Assess this cell for malaria.
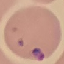

It is parasitized.

Giemsa stain. Thin blood film. Cell patch, automatically extracted from a larger field of view and resized to 64 × 64 pixels. Photographed with a smartphone camera at the microscope eyepiece.